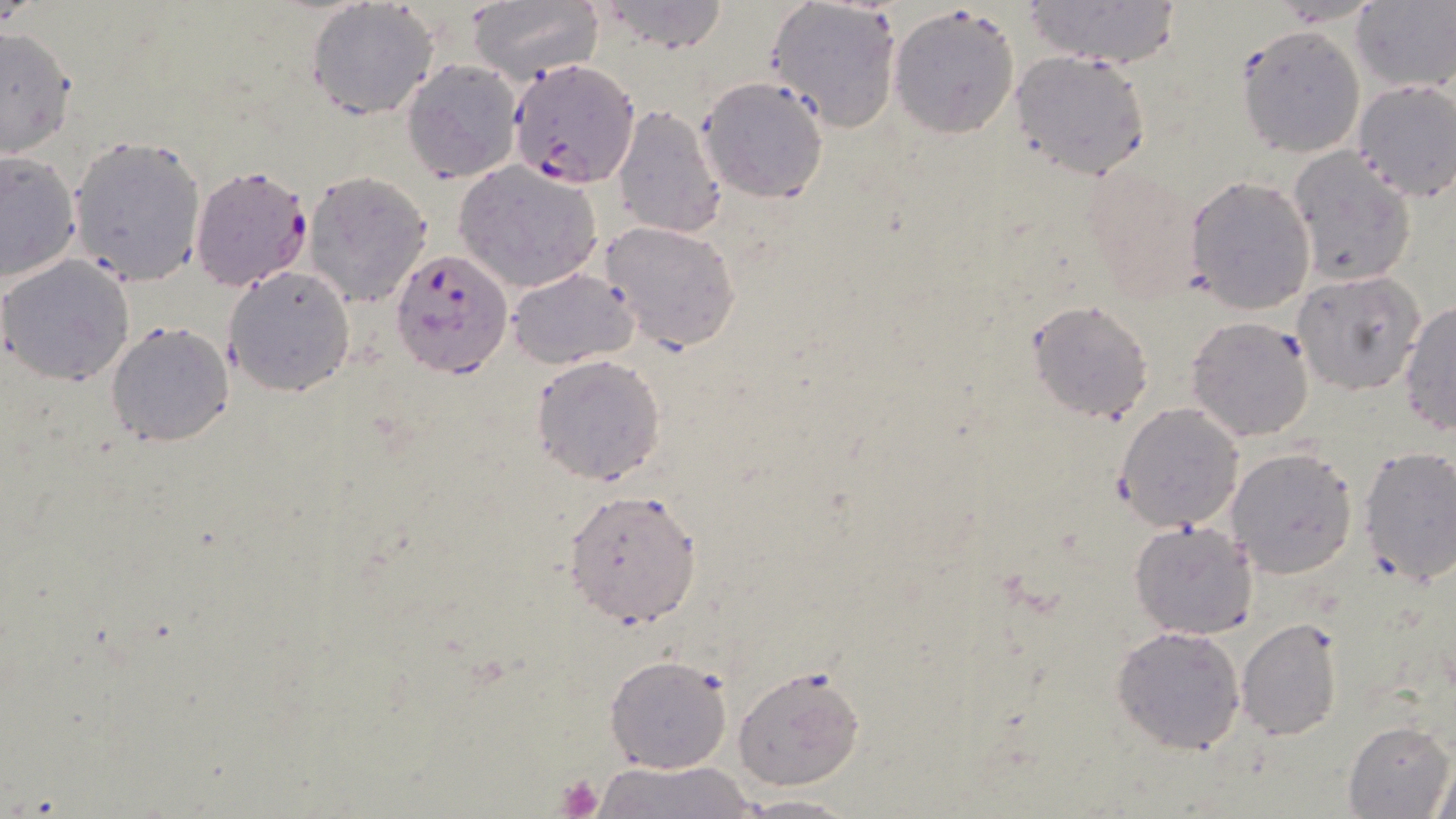

{
  "slide_level_diagnosis": "Plasmodium falciparum",
  "modality": "optical microscopy",
  "plasmodium_falciparum_infected_red_blood_cell_locations": "approximate bounding boxes as (x1, y1, x2, y2) in pixels: (511, 58, 640, 184), (188, 163, 315, 291), (389, 249, 512, 378)",
  "image_size": "1456×819 pixels",
  "preparation": "thin blood smear",
  "magnification": "1000x",
  "platelet_locations": "approximate bounding boxes as (x1, y1, x2, y2) in pixels: (554, 773, 605, 818)",
  "field_of_view": "single",
  "uninfected_red_blood_cell_locations": "approximate bounding boxes as (x1, y1, x2, y2) in pixels: (464, 0, 604, 84), (597, 0, 732, 54), (764, 0, 903, 134), (1025, 0, 1180, 69), (1351, 1, 1456, 92), (304, 3, 437, 121), (887, 3, 1022, 137), (1236, 26, 1363, 157), (0, 27, 76, 157), (1009, 48, 1155, 181), (400, 59, 522, 183), (698, 77, 829, 203), (1350, 79, 1455, 201), (613, 105, 726, 240), (67, 135, 205, 287), (1287, 146, 1416, 286), (0, 148, 82, 285), (454, 161, 604, 295), (303, 170, 434, 305), (1186, 174, 1315, 314), (599, 220, 741, 352), (1, 254, 133, 384), (225, 264, 356, 396), (507, 267, 640, 366), (1292, 272, 1426, 394), (1026, 298, 1153, 424), (1400, 298, 1456, 436), (1185, 316, 1316, 441), (107, 321, 233, 448), (530, 353, 667, 486), (1114, 401, 1245, 533), (1355, 445, 1456, 588), (1226, 446, 1358, 578), (562, 489, 703, 626), (1129, 521, 1257, 639), (1235, 617, 1345, 740), (1112, 625, 1245, 755), (604, 654, 731, 774), (733, 664, 865, 790), (1342, 721, 1453, 818), (1430, 751, 1455, 817), (599, 759, 752, 819), (731, 793, 856, 817)",
  "stain": "May-Grünwald-Giemsa"
}